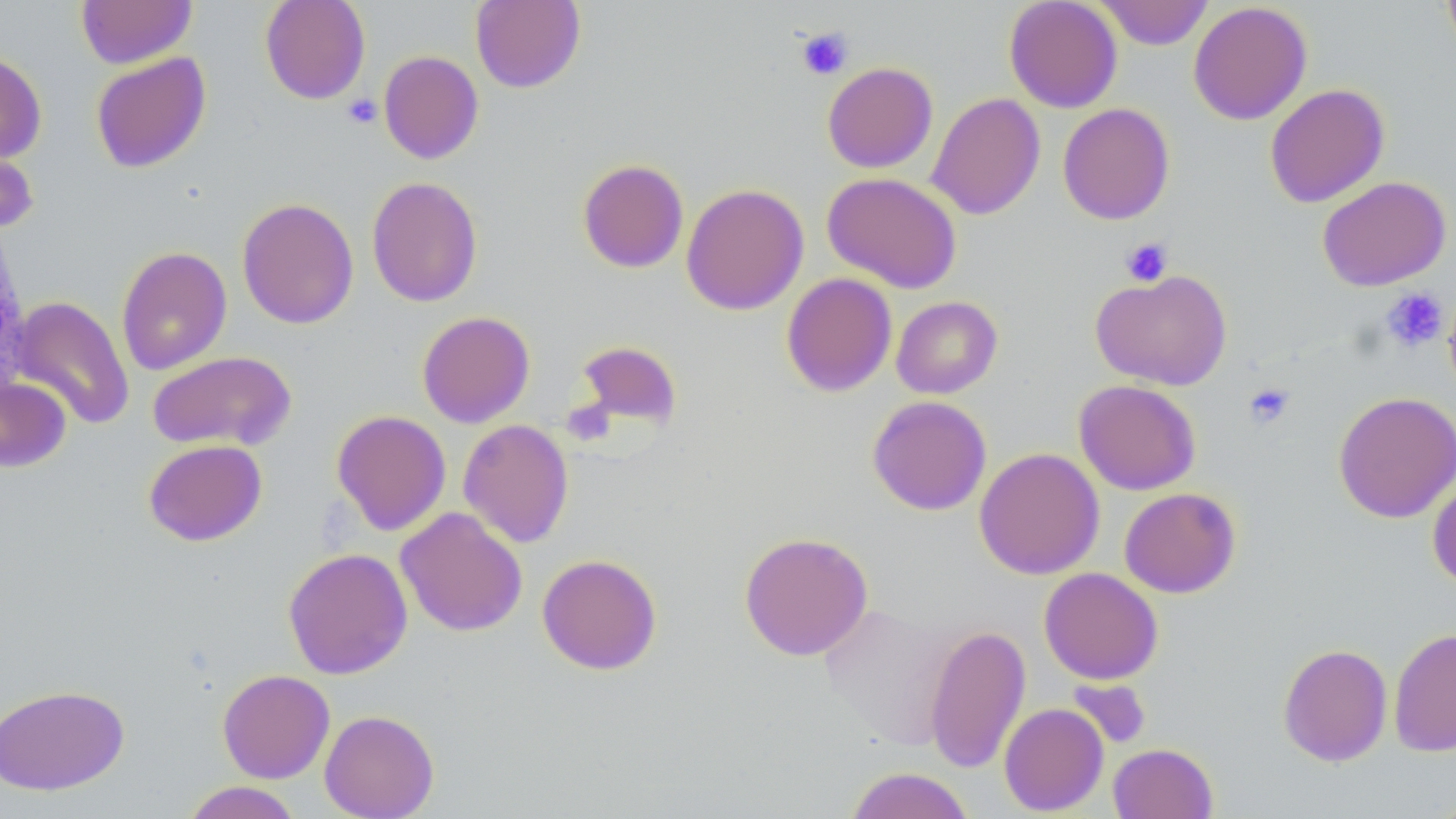 Approximate bounding boxes as [x1, y1, x2, y2] in pixels. Platelet locations: [797, 27, 853, 80], [343, 94, 383, 129], [1121, 237, 1173, 287], [1379, 287, 1450, 353], [1243, 382, 1295, 430]. Uninfected red blood cell locations: [77, 0, 197, 69], [259, 0, 371, 104], [470, 0, 586, 93], [1004, 0, 1123, 113], [1095, 0, 1214, 50], [1441, 0, 1456, 61], [1188, 2, 1312, 125], [0, 49, 47, 164], [378, 50, 484, 164], [90, 52, 212, 173], [822, 61, 938, 173], [1264, 83, 1390, 208], [927, 92, 1045, 220], [1058, 103, 1175, 225], [0, 144, 38, 233], [578, 159, 689, 273], [822, 172, 962, 293], [366, 176, 484, 307], [1317, 176, 1451, 291], [681, 183, 809, 315], [236, 197, 359, 329], [116, 246, 232, 376], [1090, 269, 1233, 390], [781, 272, 898, 397], [1443, 291, 1456, 400], [10, 295, 135, 430], [891, 296, 1003, 399], [417, 311, 535, 428], [575, 340, 684, 431], [148, 351, 297, 452], [0, 376, 71, 472], [1073, 379, 1201, 495], [1333, 391, 1456, 524], [867, 395, 992, 516], [331, 410, 451, 536], [458, 419, 574, 548], [143, 439, 267, 546], [974, 447, 1104, 580], [1427, 476, 1456, 590], [1119, 487, 1241, 598], [395, 507, 527, 637], [738, 531, 873, 661], [283, 547, 413, 680], [537, 553, 662, 675], [1039, 567, 1163, 685], [818, 602, 955, 752], [924, 624, 1031, 774], [1388, 627, 1456, 758], [1278, 643, 1393, 766], [217, 669, 335, 783], [1067, 678, 1152, 749], [0, 684, 130, 796], [998, 703, 1109, 816], [319, 709, 439, 819], [1108, 742, 1218, 819], [846, 766, 975, 819], [180, 781, 303, 819]. Slide-level diagnosis: no evidence of blood parasites. Image is 1456×819 pixels. May-Grünwald-Giemsa stain. Captured at 1000x magnification. Single field of view. Thin blood film. Optical microscopy.